Point out each leukocyte.
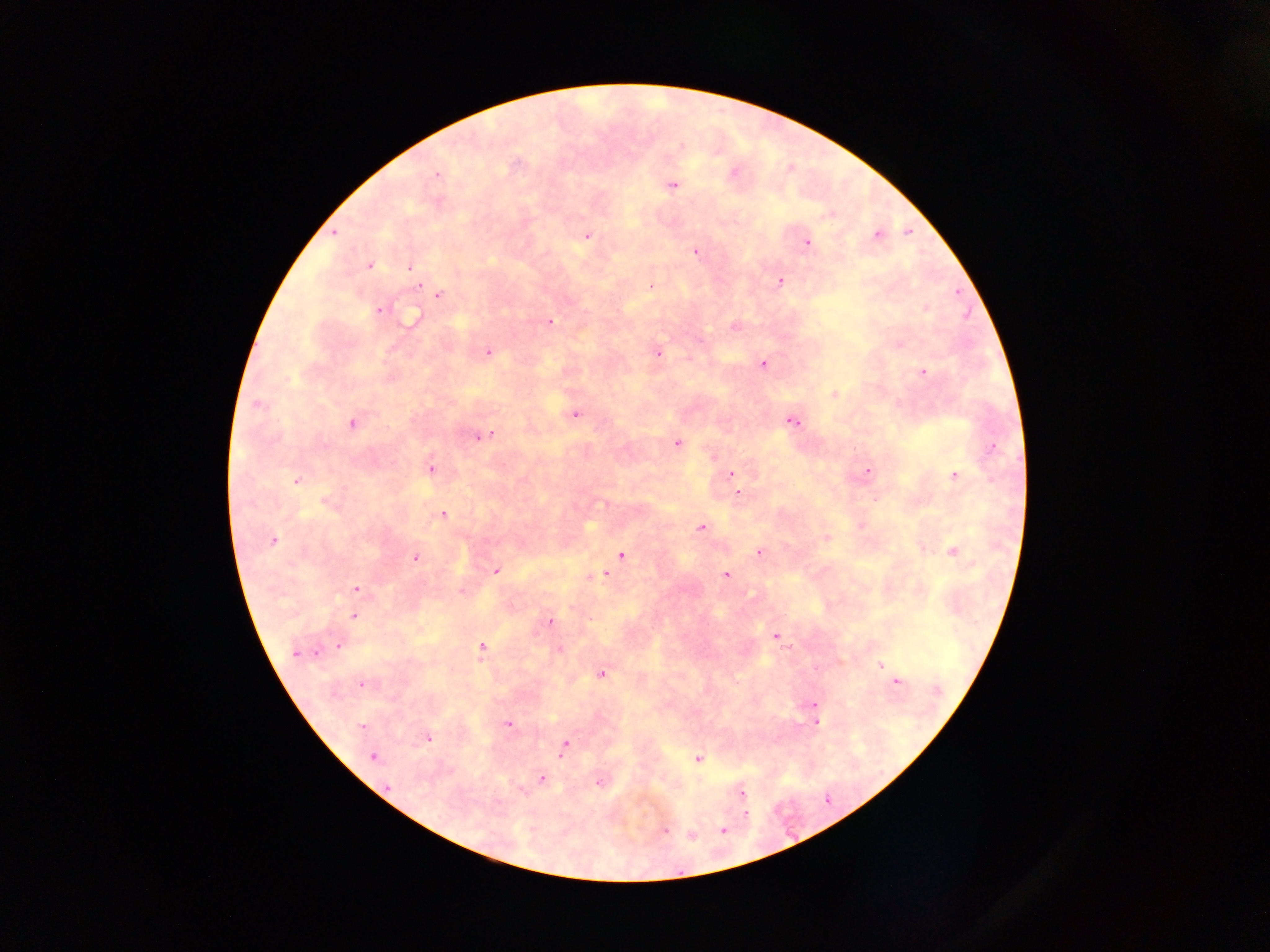
No leukocytes observed.

Approximate centers as [x, y] in pixels.
Summary:
  - Plasmodium parasite locations: [681, 147], [733, 172], [436, 174], [672, 185], [333, 232], [587, 234], [876, 234], [806, 242], [695, 250], [368, 265], [409, 267], [779, 281], [418, 285], [651, 287], [439, 294], [926, 307], [379, 309], [412, 319], [549, 321], [734, 327], [898, 343], [487, 351], [657, 352], [763, 363], [922, 372], [834, 394], [256, 405], [575, 414], [792, 421], [352, 422], [481, 435], [676, 443], [430, 468], [867, 471], [731, 474], [955, 476], [297, 480], [738, 492], [327, 502], [442, 515], [860, 524], [701, 528], [826, 537], [272, 541], [952, 550], [759, 552], [621, 556], [415, 557], [496, 570], [605, 574], [725, 575], [355, 589], [461, 591], [353, 616], [550, 620], [775, 636], [338, 644], [481, 649], [558, 649], [296, 652], [880, 665], [602, 673], [894, 677], [894, 681], [361, 684], [813, 704], [815, 721], [509, 724], [361, 727], [428, 738], [564, 745], [372, 756], [698, 759], [541, 779], [599, 781], [741, 792], [744, 813], [665, 830], [724, 830], [690, 834]
  - Image size: 1270×952 pixels
  - Country: Ghana
  - Field of view: single
  - Preparation: thick blood smear
  - Capture: mobile-phone photograph through a microscope